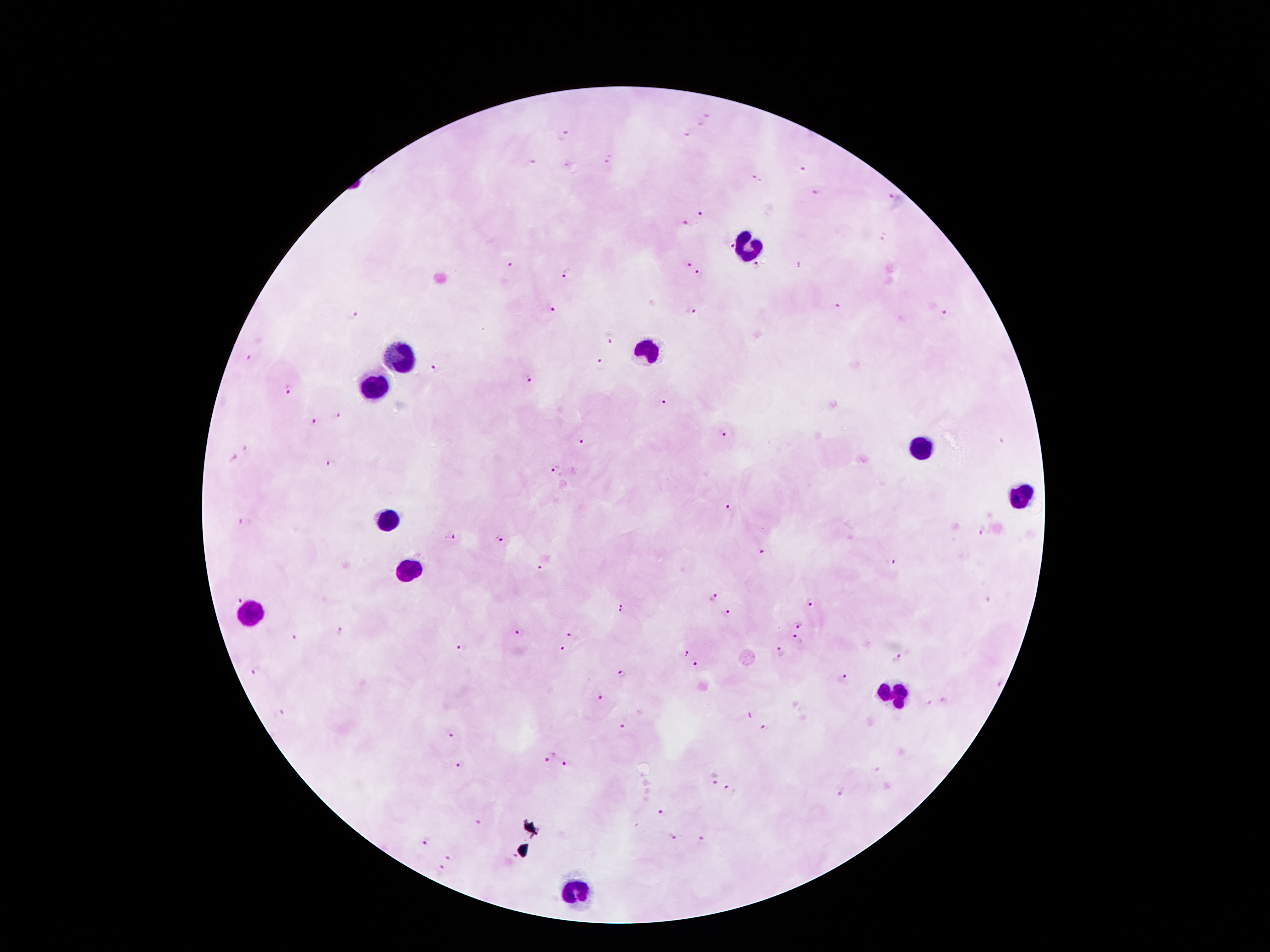

Approximate centers as [x, y] in pixels.
Summary:
  - Malaria parasite locations: [709, 117], [698, 124], [686, 134], [564, 136], [609, 160], [533, 162], [806, 169], [754, 178], [817, 192], [890, 196], [702, 210], [687, 222], [884, 238], [729, 246], [689, 263], [510, 265], [800, 266], [756, 267], [567, 274], [700, 275], [839, 305], [554, 309], [691, 311], [945, 315], [353, 316], [610, 337], [247, 359], [601, 363], [434, 370], [530, 381], [287, 390], [660, 404], [336, 416], [315, 422], [723, 433], [583, 443], [247, 447], [234, 459], [331, 464], [556, 472], [731, 507], [245, 523], [983, 530], [450, 538], [500, 538], [762, 552], [891, 561], [539, 568], [712, 597], [239, 601], [809, 603], [624, 608], [727, 612], [799, 623], [343, 634], [522, 634], [570, 636], [797, 638], [297, 639], [461, 647], [778, 651], [562, 652], [685, 652], [898, 657], [696, 666], [258, 669], [621, 674], [843, 679], [598, 698], [283, 712], [748, 717], [621, 727], [765, 728], [451, 734], [551, 757], [567, 763], [461, 765], [712, 779], [733, 790], [838, 791], [663, 814], [478, 823], [671, 838], [702, 840], [426, 842], [449, 859], [513, 859], [440, 871]
  - Leukocyte locations: [750, 247], [648, 350], [398, 353], [373, 386], [923, 445], [1020, 497], [382, 520], [405, 567], [248, 615], [891, 692], [575, 892]
  - Capture: smartphone camera through the microscope eyepiece
  - Preparation: thick blood smear
  - Patient malaria status: infected with Plasmodium falciparum
  - Stain: Giemsa
  - Field of view: one from this slide
  - Image size: 1270×952 pixels
  - Magnification: 100x